Name the cell type shown.
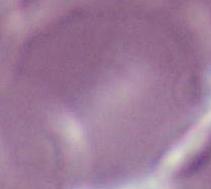

This is an erythrocyte.

Photomicrograph. 1000x magnification.